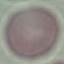

malaria status = uninfected
stain = Giemsa
capture = smartphone camera at the microscope eyepiece
preparation = thin smear
image type = cell patch, automatically extracted from a larger field of view and resized to 64 × 64 pixels